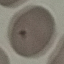

Summary:
  - Malaria status: uninfected
  - Image type: cell patch, automatically extracted from a larger field of view and resized to 64 × 64 pixels
  - Capture: smartphone through the microscope eyepiece
  - Stain: Giemsa
  - Preparation: thin smear